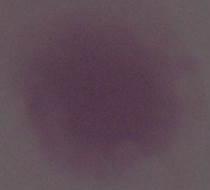

Captured at 1000x magnification. A red blood cell is seen. Photomicrograph.